Locate and identify every blood parasite.
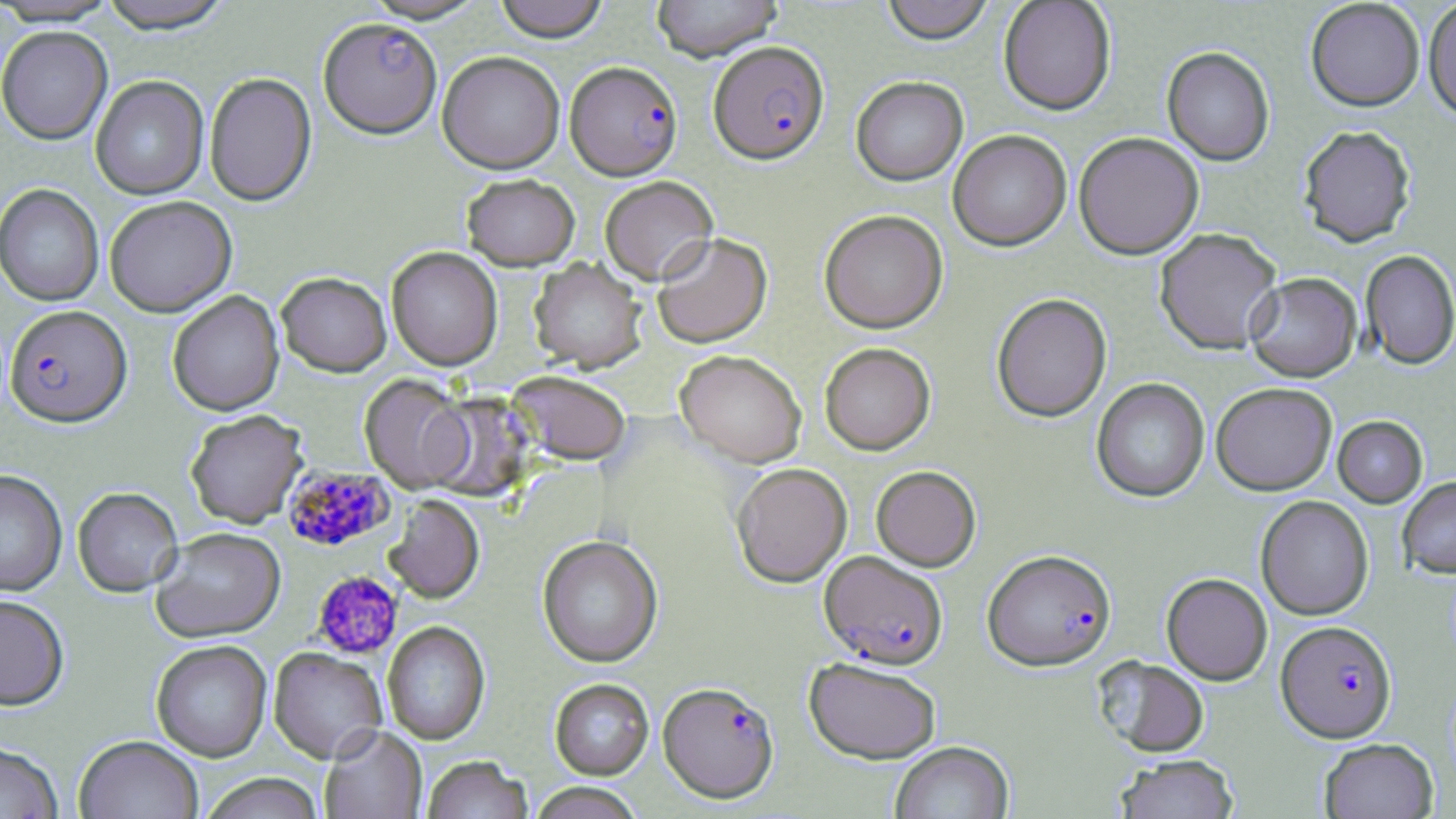

Approximate bounding boxes as named x1/y1/x2/y2 corners in pixels.
Plasmodium falciparum-infected red blood cells: (x1=318, y1=18, x2=442, y2=138), (x1=708, y1=40, x2=829, y2=164), (x1=566, y1=60, x2=682, y2=180), (x1=4, y1=305, x2=131, y2=427), (x1=281, y1=465, x2=394, y2=552), (x1=982, y1=549, x2=1116, y2=672), (x1=820, y1=551, x2=948, y2=669), (x1=1276, y1=621, x2=1396, y2=742), (x1=658, y1=681, x2=779, y2=804).
No Plasmodium ovale, Plasmodium malariae, Plasmodium vivax, Babesia divergens, or Trypanosoma brucei observed.

Platelet locations: (x1=312, y1=571, x2=404, y2=661). Uninfected red blood cell locations: (x1=0, y1=0, x2=120, y2=26), (x1=96, y1=0, x2=236, y2=34), (x1=360, y1=0, x2=489, y2=23), (x1=492, y1=0, x2=610, y2=42), (x1=652, y1=0, x2=783, y2=62), (x1=880, y1=0, x2=996, y2=44), (x1=998, y1=0, x2=1116, y2=115), (x1=1305, y1=1, x2=1424, y2=115), (x1=1423, y1=2, x2=1456, y2=126), (x1=0, y1=26, x2=113, y2=145), (x1=1161, y1=48, x2=1274, y2=167), (x1=437, y1=51, x2=565, y2=173), (x1=204, y1=73, x2=317, y2=207), (x1=91, y1=76, x2=208, y2=200), (x1=851, y1=76, x2=968, y2=186), (x1=1297, y1=128, x2=1417, y2=251), (x1=948, y1=130, x2=1072, y2=251), (x1=1073, y1=132, x2=1204, y2=259), (x1=461, y1=174, x2=580, y2=271), (x1=600, y1=176, x2=718, y2=285), (x1=0, y1=184, x2=104, y2=306), (x1=104, y1=195, x2=237, y2=317), (x1=819, y1=209, x2=948, y2=333), (x1=1154, y1=228, x2=1283, y2=355), (x1=652, y1=232, x2=772, y2=348), (x1=386, y1=246, x2=502, y2=370), (x1=1360, y1=251, x2=1456, y2=372), (x1=528, y1=258, x2=647, y2=373), (x1=277, y1=272, x2=392, y2=377), (x1=1245, y1=273, x2=1362, y2=384), (x1=168, y1=290, x2=284, y2=416), (x1=992, y1=294, x2=1112, y2=423), (x1=819, y1=343, x2=935, y2=455), (x1=675, y1=349, x2=807, y2=467), (x1=507, y1=370, x2=631, y2=465), (x1=359, y1=374, x2=471, y2=492), (x1=1091, y1=378, x2=1209, y2=503), (x1=1211, y1=384, x2=1336, y2=496), (x1=423, y1=393, x2=535, y2=503), (x1=185, y1=409, x2=307, y2=528), (x1=1332, y1=417, x2=1428, y2=509), (x1=731, y1=462, x2=852, y2=587), (x1=871, y1=465, x2=980, y2=571), (x1=0, y1=469, x2=68, y2=596), (x1=1397, y1=478, x2=1456, y2=579), (x1=72, y1=487, x2=183, y2=597), (x1=383, y1=495, x2=484, y2=603), (x1=1256, y1=496, x2=1373, y2=621), (x1=151, y1=528, x2=285, y2=642), (x1=537, y1=535, x2=663, y2=667), (x1=1161, y1=573, x2=1272, y2=685), (x1=0, y1=594, x2=69, y2=710), (x1=382, y1=622, x2=491, y2=744), (x1=151, y1=640, x2=271, y2=762), (x1=269, y1=647, x2=387, y2=763), (x1=804, y1=657, x2=940, y2=764), (x1=1095, y1=658, x2=1210, y2=758), (x1=549, y1=678, x2=654, y2=780), (x1=319, y1=726, x2=427, y2=819), (x1=74, y1=735, x2=203, y2=819), (x1=1318, y1=738, x2=1439, y2=818), (x1=0, y1=741, x2=63, y2=819), (x1=890, y1=741, x2=1014, y2=819), (x1=1114, y1=755, x2=1240, y2=819), (x1=421, y1=756, x2=533, y2=819), (x1=200, y1=773, x2=324, y2=819), (x1=528, y1=783, x2=645, y2=819). Slide-level diagnosis: Plasmodium falciparum. May-Grünwald-Giemsa stain. One field of a larger specimen. Image is 1456×819 pixels. Light microscopy. Captured at 1000x magnification. Thin blood film.